Locate every Plasmodium parasite.
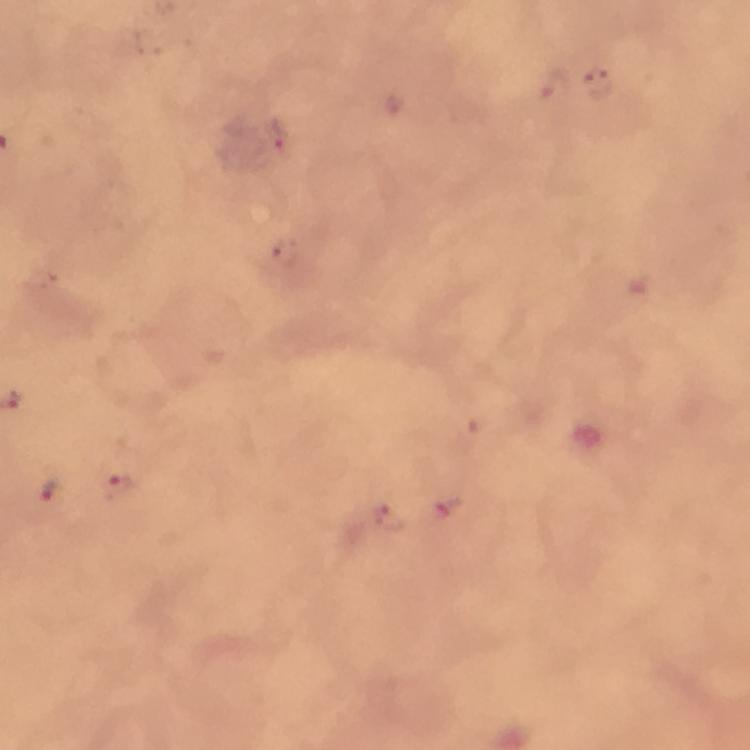
Approximate object centers, in pixels from the top-left corner.
Plasmodium parasites: (x=597, y=83), (x=278, y=135), (x=284, y=254), (x=48, y=488), (x=116, y=488), (x=448, y=509), (x=387, y=516).

From a diagnostic examination for malaria. Photographed with a smartphone mounted on the microscope. Image is 750×750 pixels. Giemsa-stained preparation. A crop from one field of view. Thick blood smear. Immersion oil was used. At 100x magnification.